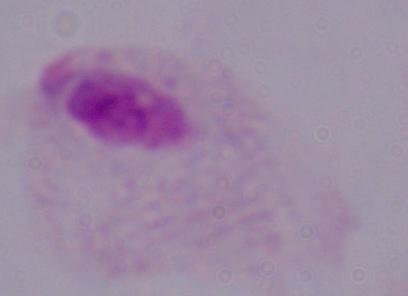

Summary:
  - Identification: trichomonad
  - Magnification: 1000x
  - Modality: micrograph